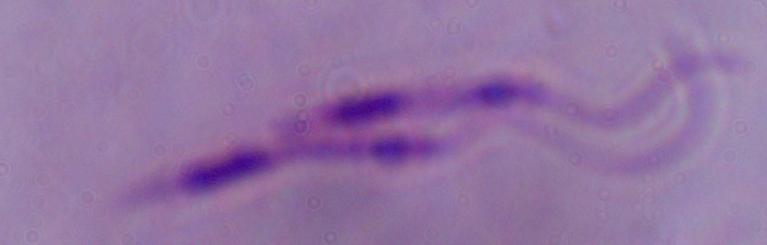

Summary:
  - Identification: Leishmania
  - Magnification: 1000x
  - Modality: micrograph